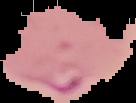

result = malaria parasites detected
image type = cell region segmented out of the field of view; surrounding area masked to black
image size = 136×103 pixels
preparation = thin blood smear